Assess the morphology of the red blood cells.
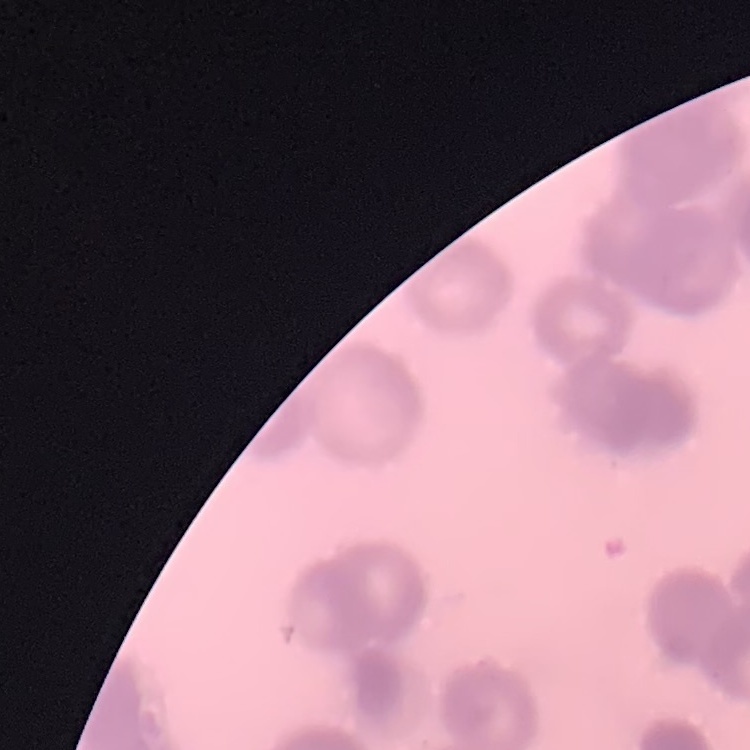

Rouleaux formation.

One tile cut from a larger photomicrograph. Thin peripheral smear. Field's or Giemsa stain.